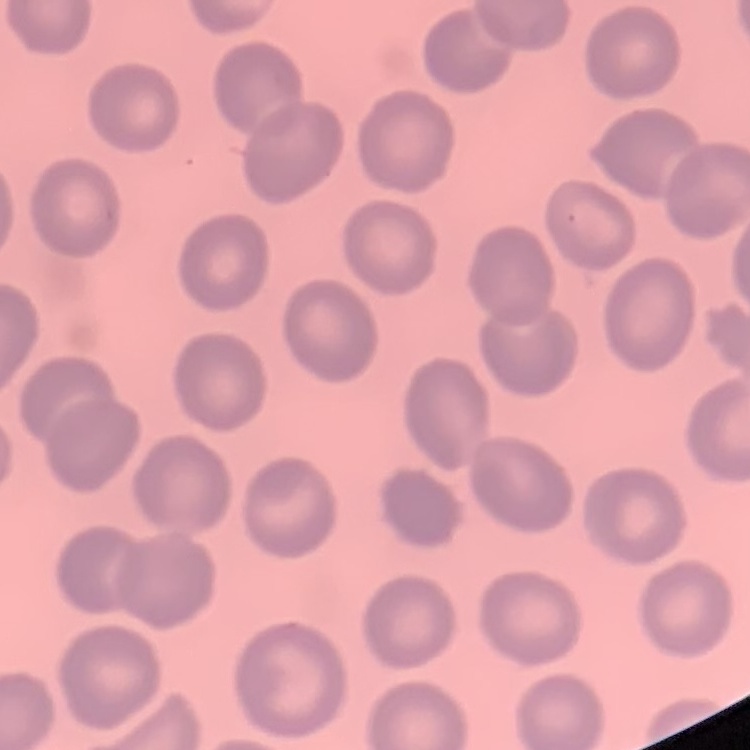

erythrocyte morphology = no rouleaux formation
stain = Field's or Giemsa
image type = square crop of a larger photomicrograph
preparation = thin peripheral smear